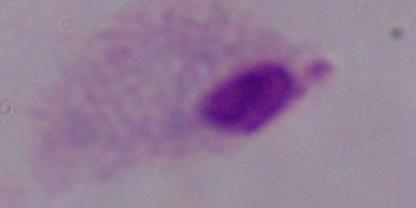
1000x magnification. Micrograph. A trichomonad is seen.